Comment on the morphology of the erythrocytes.
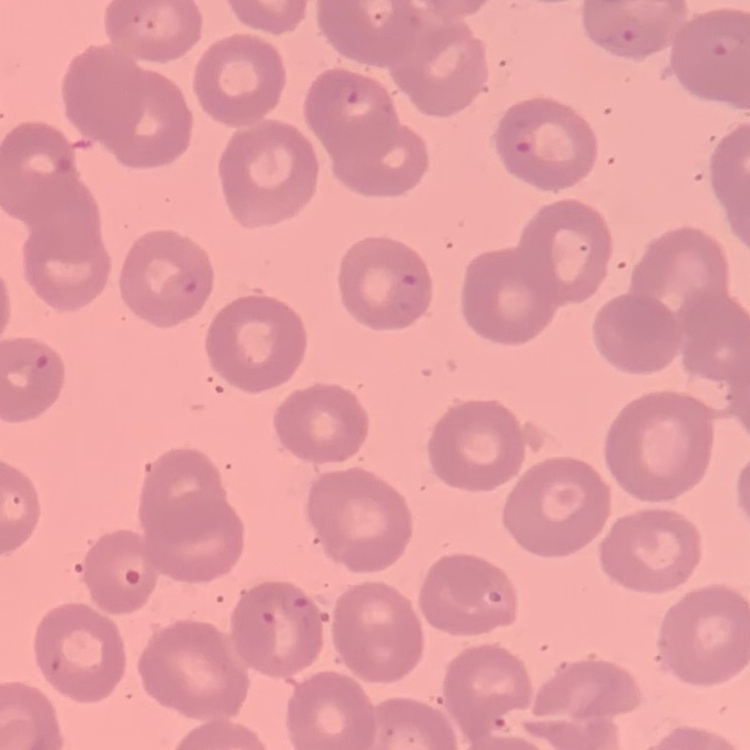

They show no rouleaux formation.

Square crop of a larger photomicrograph. Thin blood film. Stained with either Field's or Giemsa.